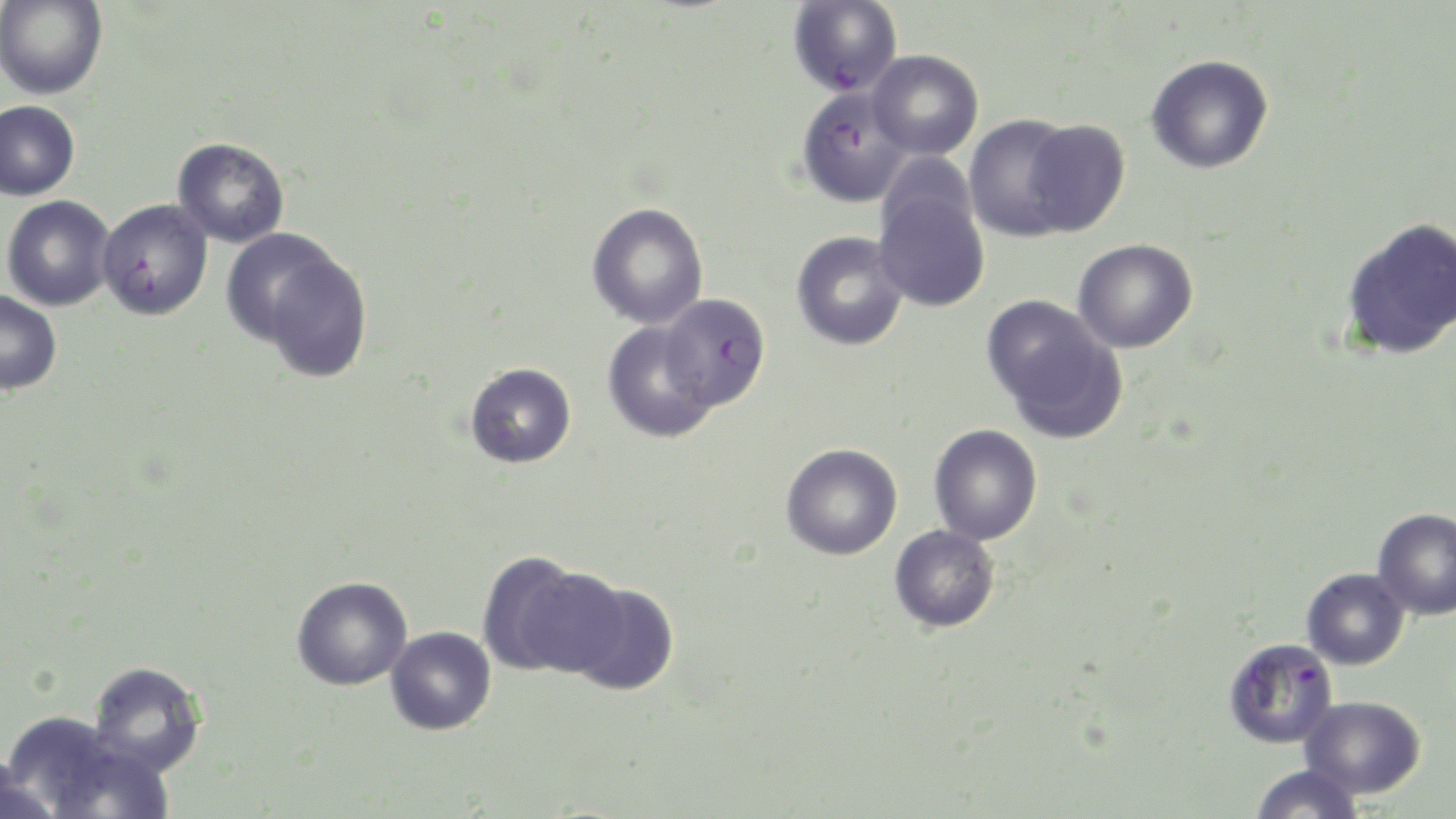
slide-level diagnosis = Plasmodium falciparum
magnification = 1000x
uninfected red blood cell locations = approximate bounding boxes as (x1, y1, x2, y2) in pixels: (0, 1, 107, 100), (867, 49, 983, 160), (1146, 54, 1274, 174), (0, 100, 80, 200), (963, 114, 1080, 241), (1021, 118, 1130, 236), (172, 136, 290, 247), (873, 182, 990, 313), (2, 195, 115, 311), (586, 202, 709, 329), (1341, 216, 1456, 360), (220, 228, 355, 350), (791, 230, 909, 351), (1073, 239, 1198, 353), (257, 249, 374, 383), (0, 290, 62, 395), (982, 294, 1127, 442), (602, 321, 718, 443), (465, 362, 577, 468), (929, 423, 1043, 545), (781, 442, 903, 560), (1372, 507, 1456, 620), (889, 525, 1000, 633), (478, 552, 617, 678), (1301, 567, 1409, 669), (292, 576, 412, 690), (561, 577, 679, 696), (385, 626, 497, 735), (88, 661, 207, 776), (1301, 695, 1426, 799), (3, 710, 147, 817), (1250, 764, 1364, 819), (0, 765, 60, 819)
modality = light microscopy
Plasmodium falciparum-infected red blood cell locations = approximate bounding boxes as (x1, y1, x2, y2) in pixels: (786, 0, 903, 97), (796, 85, 912, 209), (96, 198, 213, 320), (658, 293, 770, 411), (1223, 636, 1338, 748)
stain = May-Grünwald-Giemsa
field of view = one of a larger specimen
image size = 1456×819 pixels
preparation = thin blood film